Locate every Plasmodium parasite.
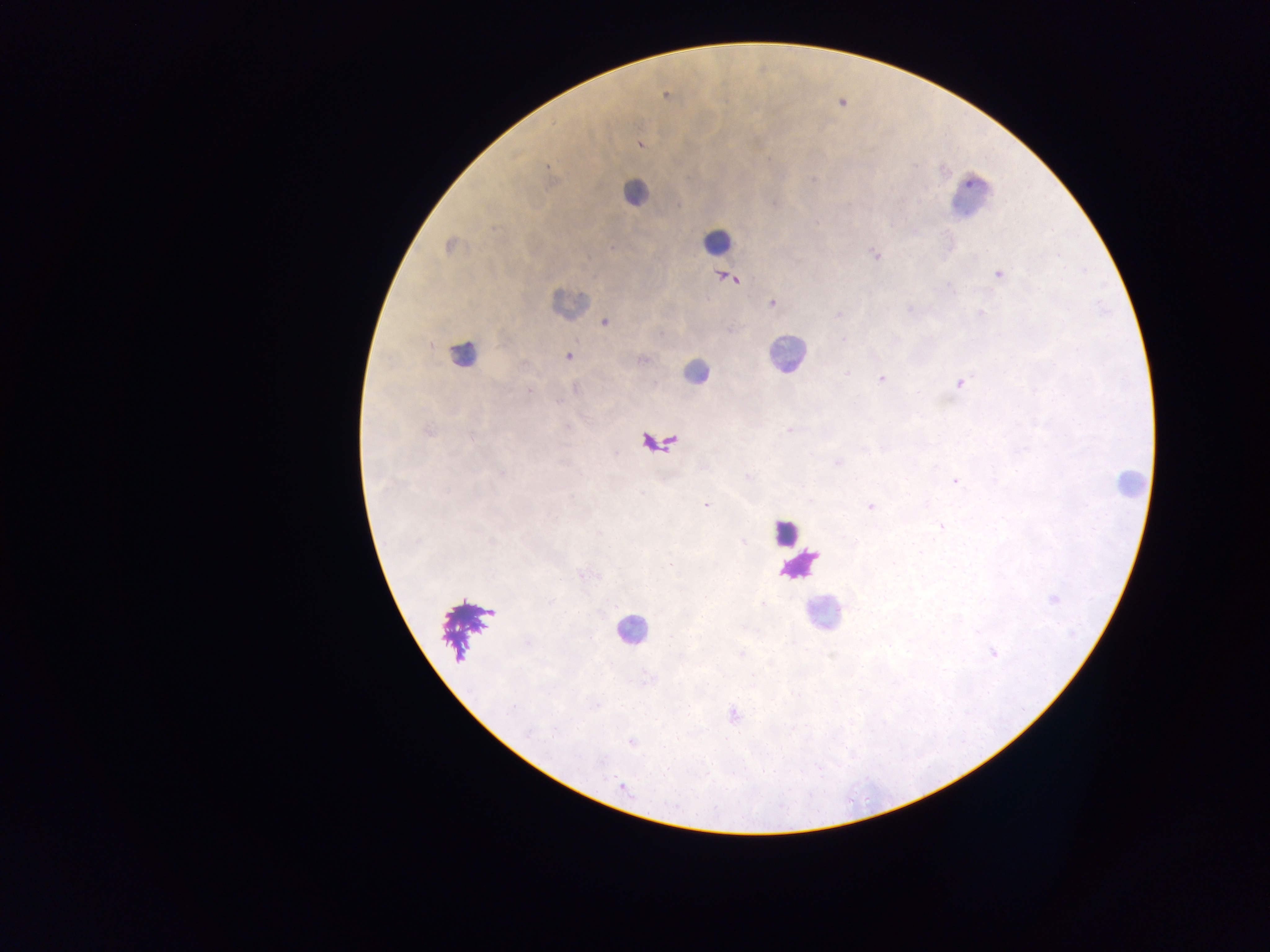

Approximate centers as (x, y) in pixels.
Plasmodium parasites: (666, 96), (639, 144), (448, 246), (613, 247), (875, 254), (1058, 255), (998, 274), (730, 277), (948, 285), (772, 304), (909, 309), (980, 313), (838, 315), (605, 323), (843, 340), (568, 357), (643, 359), (846, 373), (881, 379), (960, 384), (529, 390), (789, 430), (429, 431), (838, 463), (748, 477), (955, 481), (706, 506), (870, 507), (941, 526), (492, 541), (743, 543), (670, 564), (1054, 599), (550, 602), (763, 604), (993, 653), (597, 705), (512, 708), (733, 715), (530, 732), (632, 743), (622, 786).

Leukocyte locations: (634, 193), (970, 195), (717, 241), (568, 303), (461, 354), (785, 354), (695, 372), (1129, 482), (785, 532), (822, 614), (631, 630). Sample from Ghana. Thick blood film. One field of view. Photographed through a microscope with a mobile-phone camera. Image is 1270×952 pixels.